Describe the morphology of the red blood cells.
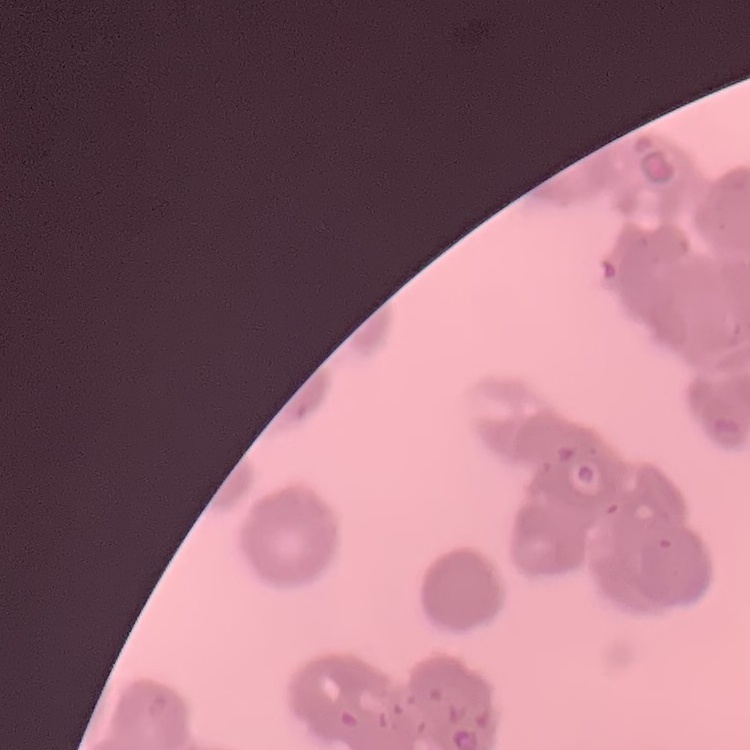
Rouleaux formation.

preparation = thin blood smear
image type = square crop of a larger photomicrograph
stain = Field's or Giemsa